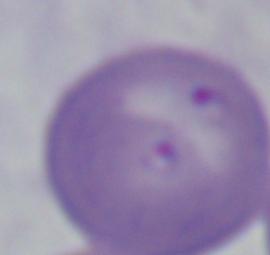
Summary:
  - Modality: micrograph
  - Magnification: 1000x
  - Identification: Babesia